Give the extent of all Plasmodium falciparum-infected red blood cells.
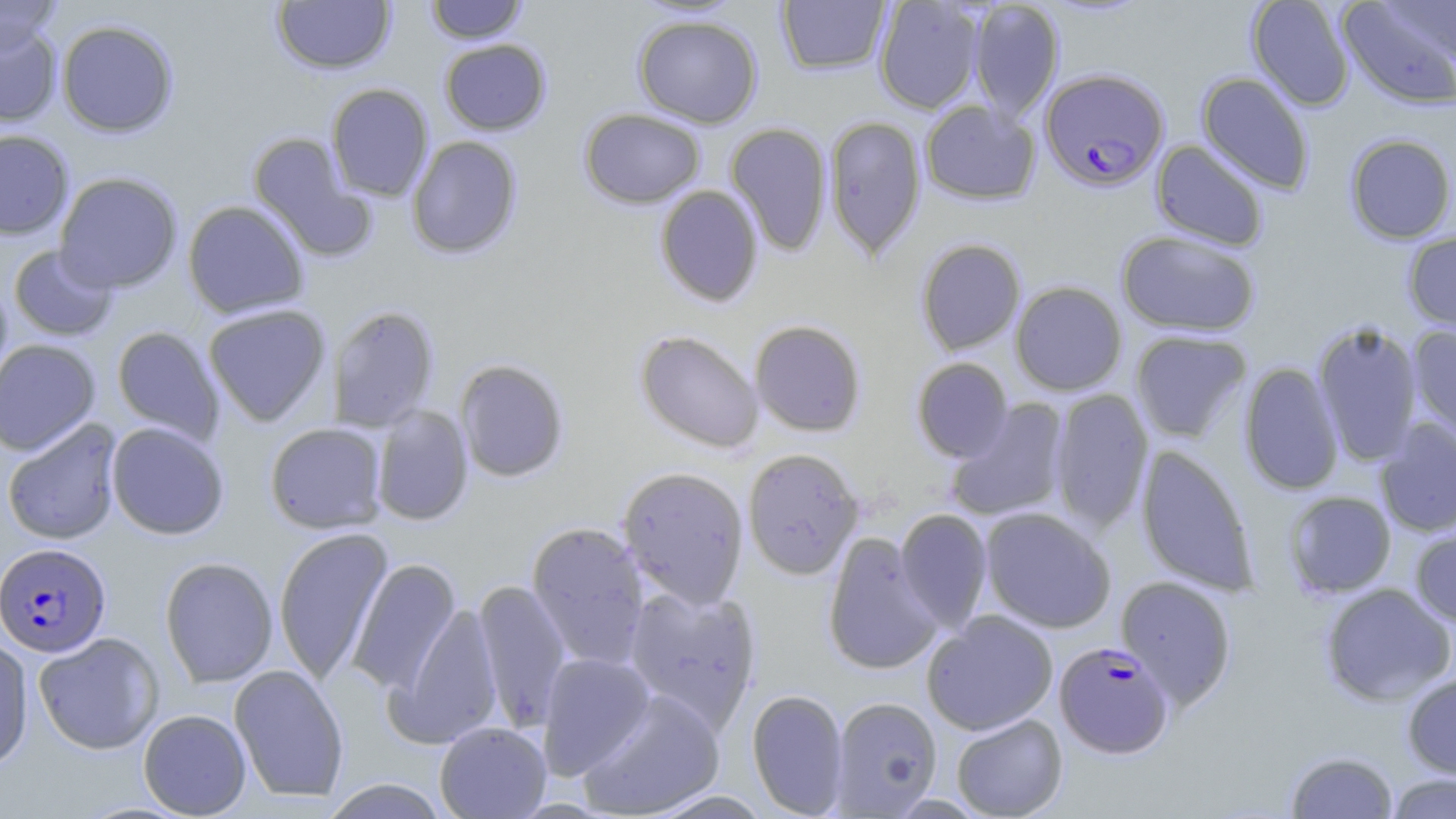

Approximate bounding boxes as [x1, y1, x2, y2] in pixels.
Plasmodium falciparum-infected red blood cells: [1039, 68, 1169, 191], [0, 541, 106, 656], [1054, 641, 1174, 759].

Summary:
  - Uninfected red blood cell locations: [0, 0, 62, 57], [425, 0, 528, 43], [873, 0, 984, 114], [1246, 0, 1355, 111], [1338, 0, 1456, 109], [272, 1, 396, 74], [776, 1, 891, 75], [967, 1, 1065, 122], [633, 14, 763, 128], [56, 19, 179, 137], [0, 21, 63, 128], [439, 39, 551, 136], [1196, 72, 1314, 195], [326, 83, 434, 203], [920, 100, 1040, 205], [579, 108, 706, 208], [823, 115, 926, 261], [725, 122, 833, 257], [0, 129, 74, 240], [247, 132, 375, 262], [1344, 133, 1456, 244], [407, 136, 523, 259], [1151, 140, 1269, 250], [54, 172, 183, 293], [654, 185, 764, 307], [183, 200, 310, 319], [1116, 230, 1261, 336], [1403, 230, 1456, 338], [916, 238, 1026, 356], [9, 244, 119, 342], [0, 276, 13, 390], [1010, 281, 1127, 396], [203, 303, 332, 426], [327, 305, 440, 432], [749, 319, 867, 437], [1312, 321, 1423, 467], [1407, 324, 1456, 442], [111, 326, 224, 444], [635, 329, 764, 453], [1130, 330, 1251, 443], [0, 339, 101, 456], [911, 357, 1013, 462], [454, 359, 569, 482], [1238, 362, 1344, 496], [1049, 389, 1153, 534], [945, 399, 1071, 522], [371, 404, 474, 526], [2, 419, 123, 545], [1375, 419, 1456, 537], [106, 422, 230, 540], [265, 422, 387, 534], [1135, 445, 1259, 596], [742, 447, 864, 580], [617, 466, 750, 608], [1283, 491, 1396, 597], [979, 507, 1116, 634], [895, 509, 993, 631], [526, 521, 650, 671], [1410, 525, 1456, 628], [273, 527, 393, 684], [822, 533, 944, 676], [159, 556, 279, 687], [347, 558, 461, 696], [1116, 575, 1237, 709], [473, 578, 572, 732], [623, 583, 762, 732], [1320, 583, 1455, 706], [387, 601, 503, 748], [921, 611, 1058, 735], [33, 632, 164, 755], [0, 636, 34, 775], [537, 652, 655, 779], [228, 665, 349, 802], [1402, 672, 1456, 780], [576, 689, 726, 817], [747, 689, 849, 817], [830, 696, 942, 816], [138, 709, 251, 818], [951, 714, 1068, 818], [435, 722, 551, 818], [1285, 750, 1398, 818], [1386, 773, 1455, 818], [321, 779, 449, 819], [647, 789, 772, 818]
  - Slide-level diagnosis: Plasmodium falciparum
  - Stain: May-Grünwald-Giemsa
  - Field of view: single
  - Preparation: thin blood smear
  - Image size: 1456×819 pixels
  - Magnification: 1000x
  - Modality: optical microscopy